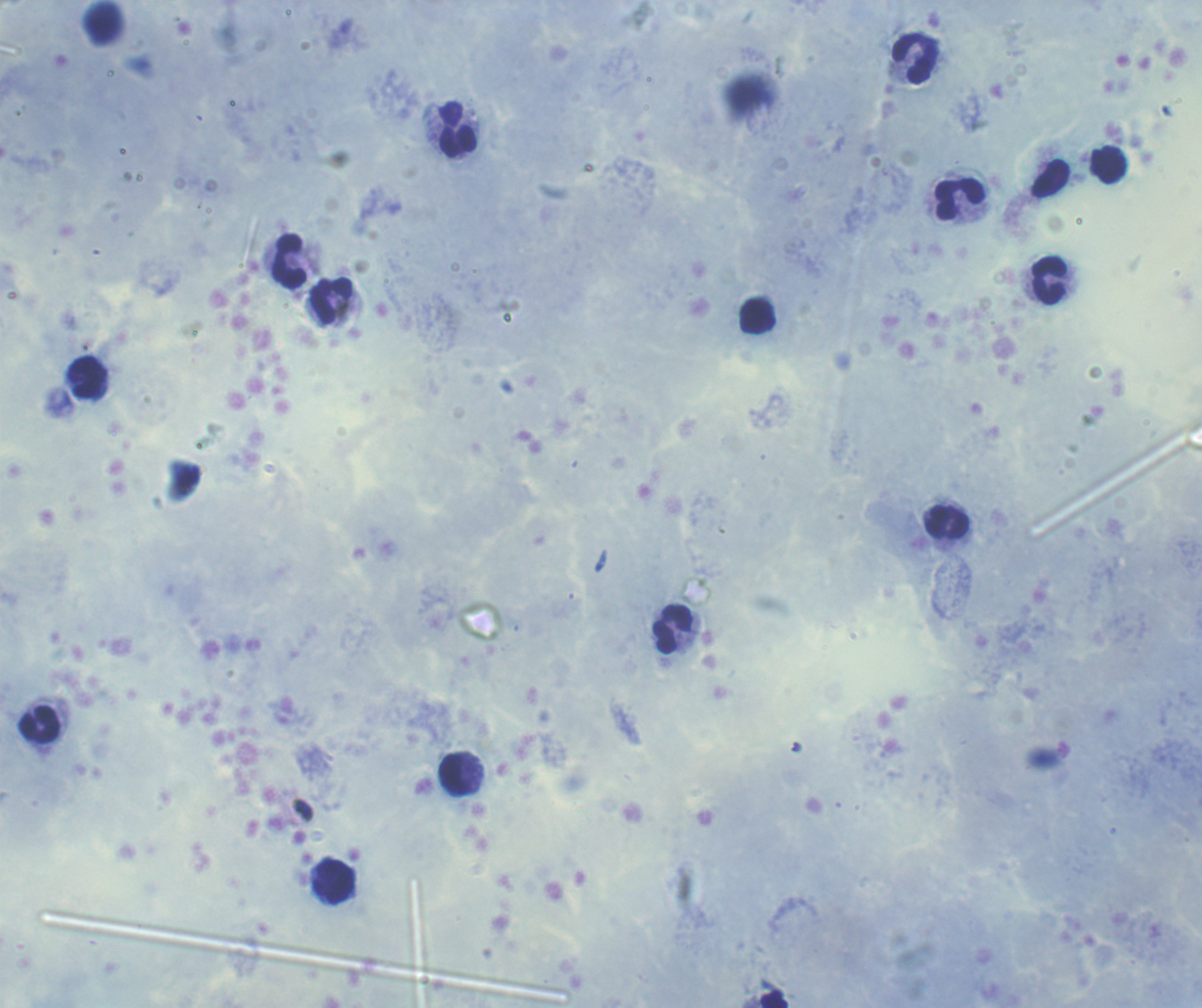
Approximate centers as (x, y) in pixels. Leukocyte locations: (916, 58), (457, 130), (1108, 165), (960, 198), (288, 261), (1048, 281), (331, 301), (757, 317), (86, 378), (947, 523), (671, 629), (39, 725), (455, 774), (334, 882), (774, 998). Previously used in a real diagnosis. Thick smear of blood. Coloration quality: good. Background quality: satisfactory. Single field of view. Image is 1202×1008 pixels. 100x magnification. Result: no malaria parasites detected. Romanowsky stain.